Identify the cell.
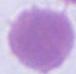
An erythrocyte.

Summary:
  - Modality: photomicrograph
  - Magnification: 1000x